Report the malaria status of this cell.
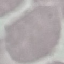

Uninfected.

Summary:
  - Preparation: thin smear
  - Image type: cell patch, automatically extracted from a larger field of view and resized to 64 × 64 pixels
  - Stain: Giemsa
  - Capture: smartphone through the microscope eyepiece